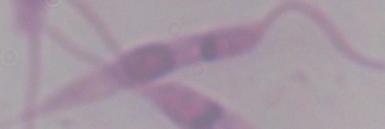
Summary:
  - Magnification: 1000x
  - Identification: Leishmania
  - Modality: photomicrograph